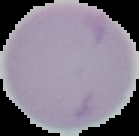

Summary:
  - Malaria status: uninfected
  - Preparation: thin blood smear
  - Image size: 139×136 pixels
  - Image type: segmented cell region with the area outside set to black